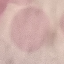

Malaria status: uninfected. Photographed with a smartphone camera at the microscope eyepiece. Giemsa-stained preparation. Cell patch, automatically extracted from a larger field of view and resized to 64 × 64 pixels. Thin blood film.